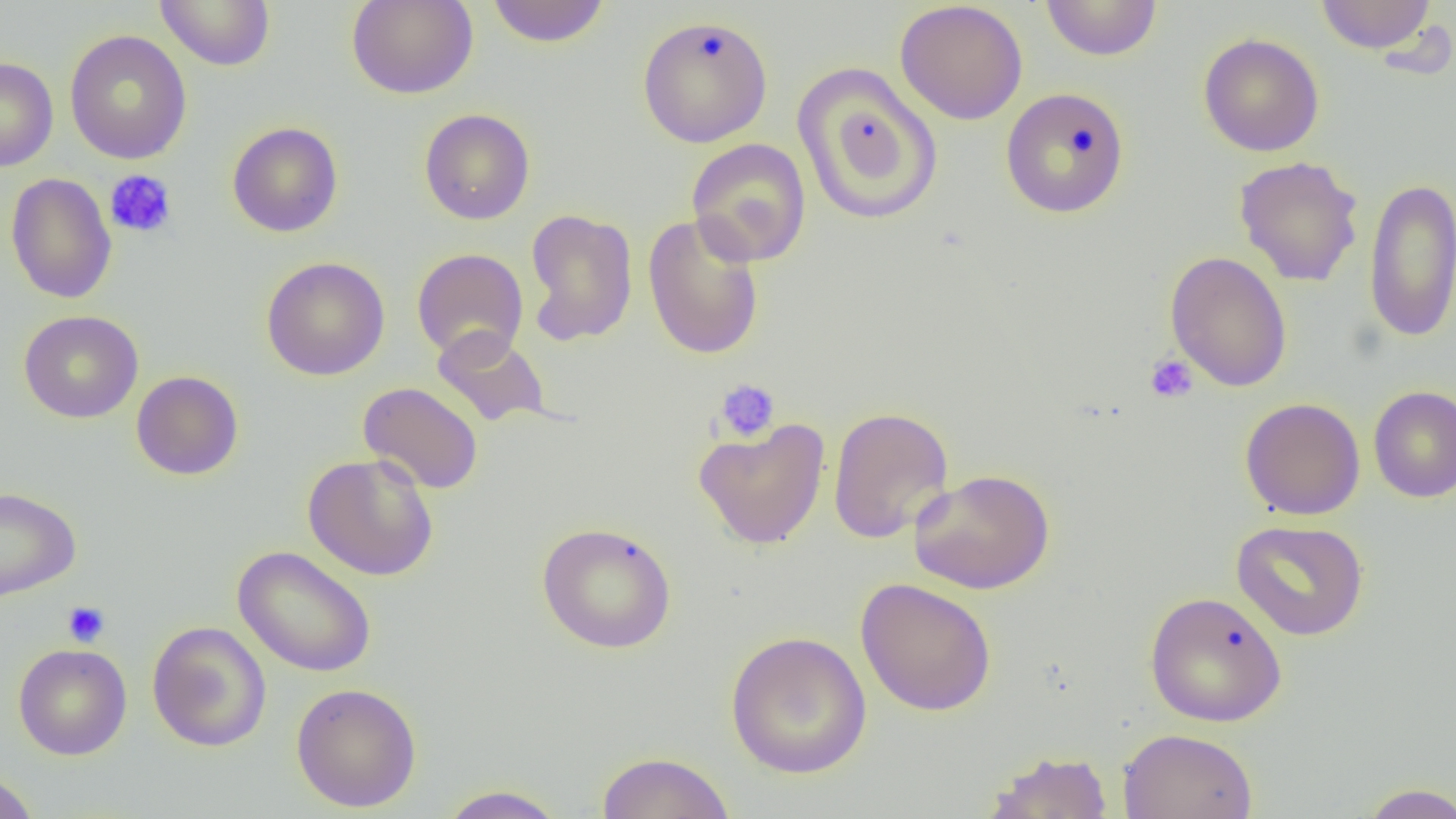

slide-level diagnosis = no evidence of blood parasites
field of view = one of a larger specimen
modality = light microscopy
uninfected red blood cell locations = approximate bounding boxes as [x1, y1, x2, y2] in pixels: [156, 0, 276, 71], [346, 0, 479, 99], [486, 0, 611, 48], [1040, 0, 1163, 61], [1315, 0, 1436, 53], [894, 1, 1028, 125], [636, 14, 774, 148], [64, 29, 193, 165], [1198, 32, 1325, 157], [0, 57, 58, 172], [792, 63, 942, 225], [1000, 87, 1130, 218], [419, 108, 535, 225], [227, 121, 343, 238], [686, 138, 811, 267], [1233, 155, 1364, 287], [5, 173, 118, 304], [1363, 177, 1456, 343], [523, 208, 638, 347], [642, 212, 766, 361], [411, 248, 528, 362], [1165, 251, 1292, 392], [261, 256, 390, 381], [18, 309, 144, 424], [432, 326, 552, 428], [131, 370, 244, 480], [358, 381, 484, 495], [1368, 386, 1456, 503], [1240, 397, 1366, 520], [828, 406, 954, 543], [693, 417, 831, 549], [303, 453, 440, 581], [909, 468, 1055, 595], [0, 486, 81, 602], [1231, 519, 1369, 641], [536, 521, 676, 654], [232, 545, 376, 678], [856, 577, 997, 717], [1144, 591, 1288, 727], [147, 621, 271, 752], [724, 630, 872, 779], [13, 643, 132, 760], [291, 682, 422, 812], [1117, 727, 1258, 819], [982, 750, 1114, 819], [596, 751, 736, 818], [0, 769, 40, 819], [1356, 782, 1456, 819], [436, 784, 570, 818]
platelet locations = approximate bounding boxes as [x1, y1, x2, y2] in pixels: [104, 170, 177, 239], [1145, 354, 1199, 404], [714, 378, 781, 443], [62, 601, 110, 647]
preparation = thin blood film
image size = 1456×819 pixels
magnification = 1000x